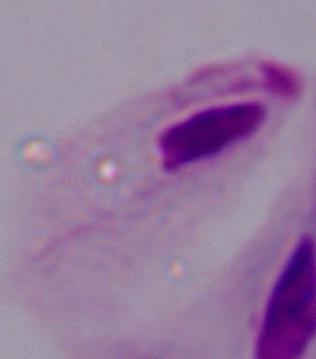

Summary:
  - Magnification: 1000x
  - Identification: trichomonad
  - Modality: micrograph